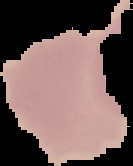
The area outside the segmented cell region is set to black. From a thin blood film. Result: negative for malaria parasites. Image is 133×166 pixels.